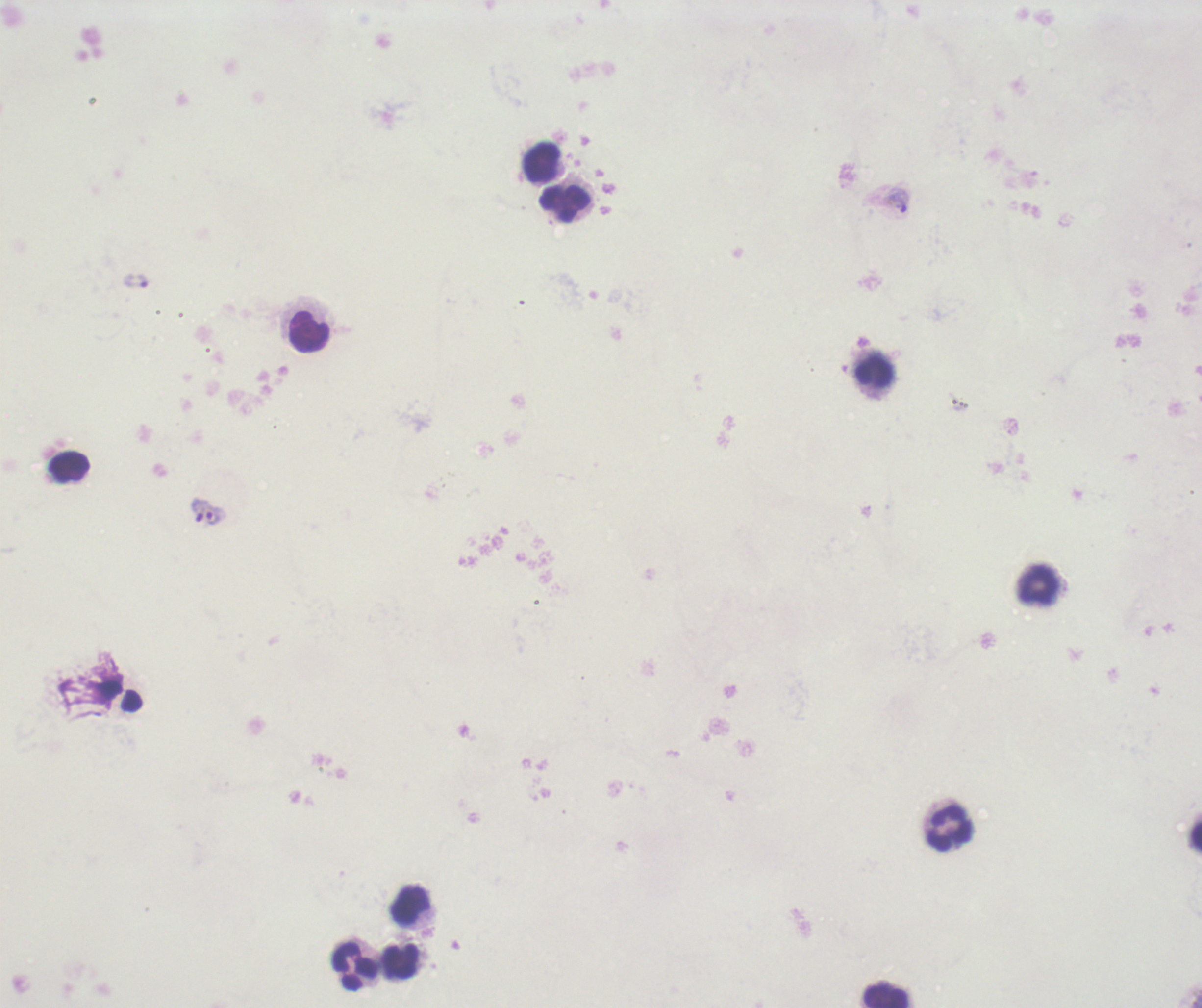
image_size: 1202×1008 pixels
magnification: 100x
context: previously used in a real diagnosis
result: Plasmodium parasites identified
stain: Romanowsky
coloration_quality: bad
trophozoite_locations: 'approximate object centers, in pixels from the top-left corner: (x=897, y=199), (x=137, y=281), (x=199, y=510), (x=214, y=515)'
leukocyte_locations: 'approximate object centers, in pixels from the top-left corner: (x=542, y=162), (x=564, y=203), (x=310, y=333), (x=874, y=370), (x=70, y=467), (x=1038, y=585), (x=949, y=827), (x=410, y=906), (x=401, y=962), (x=355, y=966), (x=886, y=995)'
field_of_view: single
background_quality: poor
preparation: thick smear of blood